Give the preparation type.
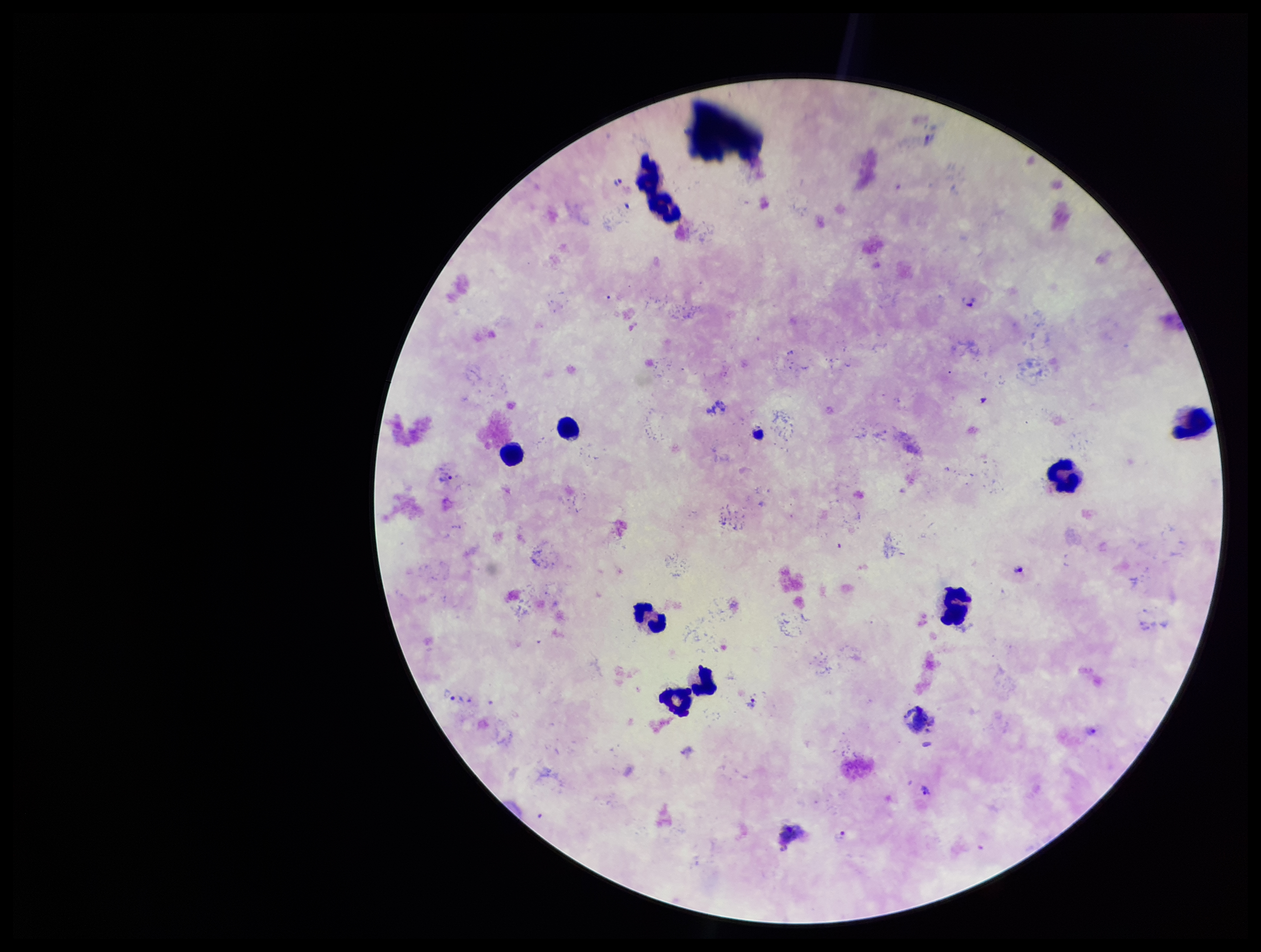

Thick.

{
  "field_of_view": "one from this slide",
  "plasmodium_parasites": "seen",
  "capture": "smartphone photograph through the microscope eyepiece",
  "species_reported_for_this_patient": "Plasmodium vivax",
  "image_size": "1261×952 pixels",
  "leukocyte_count": 9,
  "patient_malaria_status": "infected",
  "stain": "Giemsa",
  "parasite_count": 3
}